Report the malaria status of this cell.
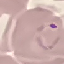
It is parasitized.

Summary:
  - Capture: smartphone through the microscope eyepiece
  - Preparation: thin blood smear
  - Stain: Giemsa
  - Image type: cell patch, automatically extracted from a larger field of view and resized to 64 × 64 pixels